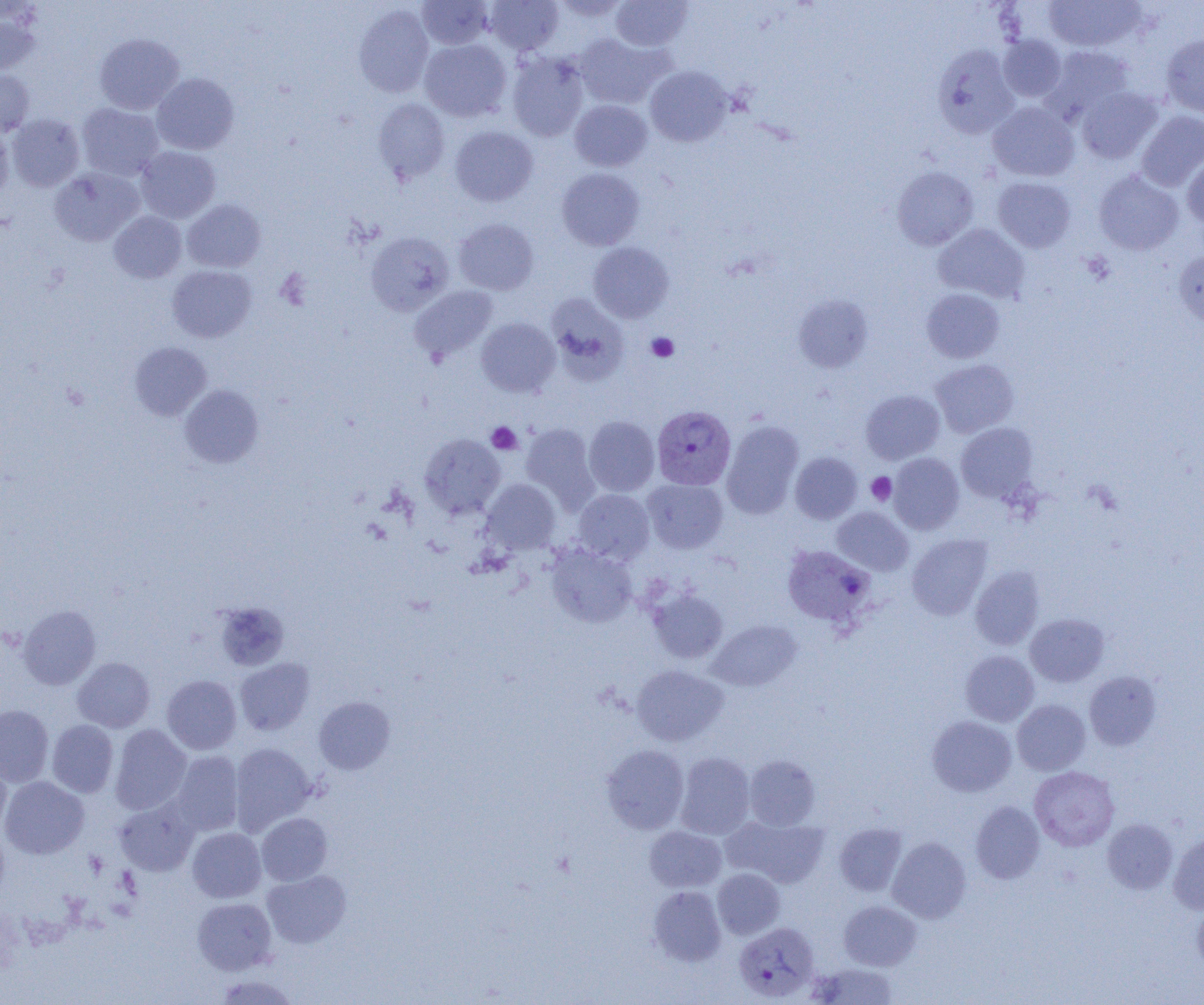

Summary:
  - Coordinate format: approximate bounding boxes as (x1, y1, x2, y2) in pixels
  - Plasmodium vivax-infected red blood cell locations (subset): (652, 405, 736, 490), (782, 544, 874, 626)
  - Uninfected red blood cell locations (subset): (485, 0, 562, 54), (550, 0, 631, 22), (1044, 0, 1145, 51), (417, 1, 494, 49), (611, 1, 692, 51), (354, 5, 434, 98), (0, 10, 40, 75), (94, 33, 184, 114), (575, 33, 671, 109), (998, 35, 1066, 102), (1161, 35, 1204, 117), (419, 39, 512, 121), (932, 44, 1020, 138), (1044, 46, 1133, 121), (507, 52, 589, 142), (645, 65, 733, 147), (0, 70, 34, 135), (152, 73, 239, 154), (1077, 87, 1162, 163), (373, 99, 450, 183), (570, 100, 652, 171), (988, 102, 1079, 182), (76, 103, 163, 181), (1136, 111, 1204, 191), (7, 113, 84, 192), (0, 122, 13, 203), (450, 125, 538, 206), (136, 146, 220, 223), (1182, 153, 1204, 229), (892, 166, 978, 250), (557, 167, 644, 250), (49, 168, 144, 246), (1094, 170, 1184, 255), (993, 177, 1075, 252), (182, 199, 266, 273), (109, 211, 186, 283), (454, 218, 539, 295), (934, 224, 1029, 303), (365, 231, 455, 315), (588, 242, 674, 323), (1173, 250, 1204, 329), (167, 265, 256, 343), (410, 286, 498, 362), (921, 288, 1004, 363), (546, 294, 629, 384), (793, 295, 873, 372), (476, 317, 560, 396), (129, 342, 211, 420), (931, 359, 1018, 438), (179, 384, 264, 468), (861, 389, 944, 464), (583, 416, 659, 496), (722, 420, 804, 519), (520, 422, 599, 511), (956, 423, 1037, 502), (419, 433, 505, 518), (790, 452, 862, 524), (888, 453, 964, 534), (642, 478, 728, 554), (481, 479, 561, 554), (574, 489, 655, 563), (831, 507, 913, 575), (907, 534, 993, 619), (547, 543, 637, 627), (970, 567, 1044, 650), (648, 588, 728, 664), (18, 604, 101, 690), (221, 604, 295, 673), (1025, 613, 1109, 687), (708, 620, 801, 691), (960, 650, 1039, 726), (73, 657, 155, 732), (235, 658, 315, 736), (631, 665, 728, 746), (1084, 671, 1161, 750), (162, 675, 241, 754), (314, 697, 396, 775), (1012, 700, 1090, 775), (0, 705, 53, 786), (927, 715, 1017, 796), (47, 720, 118, 797), (110, 724, 192, 814), (229, 743, 317, 834), (601, 745, 689, 834), (171, 751, 244, 836), (675, 752, 756, 839), (744, 755, 820, 830), (0, 758, 12, 836), (1030, 766, 1119, 851), (0, 776, 89, 859), (114, 796, 200, 876), (970, 801, 1044, 883), (256, 813, 333, 886), (722, 815, 829, 888), (1102, 819, 1178, 894), (834, 823, 907, 896), (0, 826, 10, 905), (644, 826, 726, 892), (187, 827, 265, 902), (1168, 832, 1204, 914), (887, 836, 971, 923), (713, 868, 784, 939), (262, 870, 351, 948), (648, 886, 726, 965), (192, 897, 277, 974), (839, 901, 921, 970), (1192, 901, 1204, 976), (809, 962, 897, 1004), (213, 974, 300, 1004)
  - Platelet locations: (646, 333, 679, 362), (486, 421, 522, 454), (867, 472, 896, 505)
  - Slide-level diagnosis: Plasmodium vivax
  - Preparation: thin blood smear
  - Field of view: one of a larger specimen
  - Image size: 1204×1005 pixels
  - Modality: light microscopy
  - Magnification: 1000x